Classify this cell by malaria status.
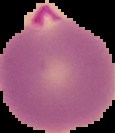
Parasitized.

image type = segmented cell region on a black background
preparation = thin blood smear
image size = 115×133 pixels